Classify this cell by malaria status.
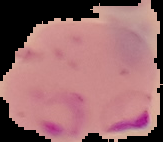
It is parasitized.

{
  "image_type": "segmented cell region with the area outside set to black",
  "image_size": "163×142 pixels",
  "preparation": "thin blood smear"
}